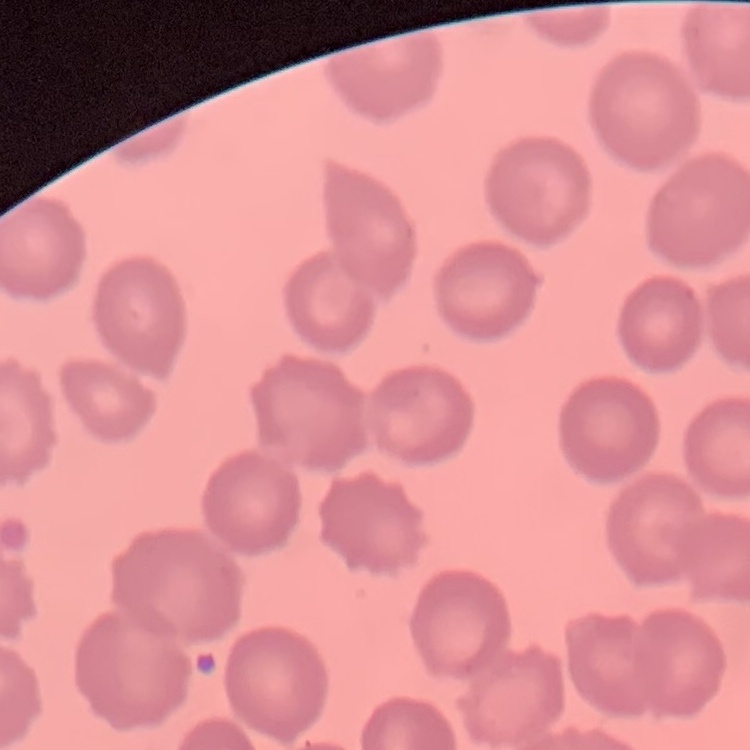
red blood cell morphology = no rouleaux formation
image type = square crop of a larger photomicrograph
stain = Field's or Giemsa
preparation = thin blood smear